Locate every white blood cell.
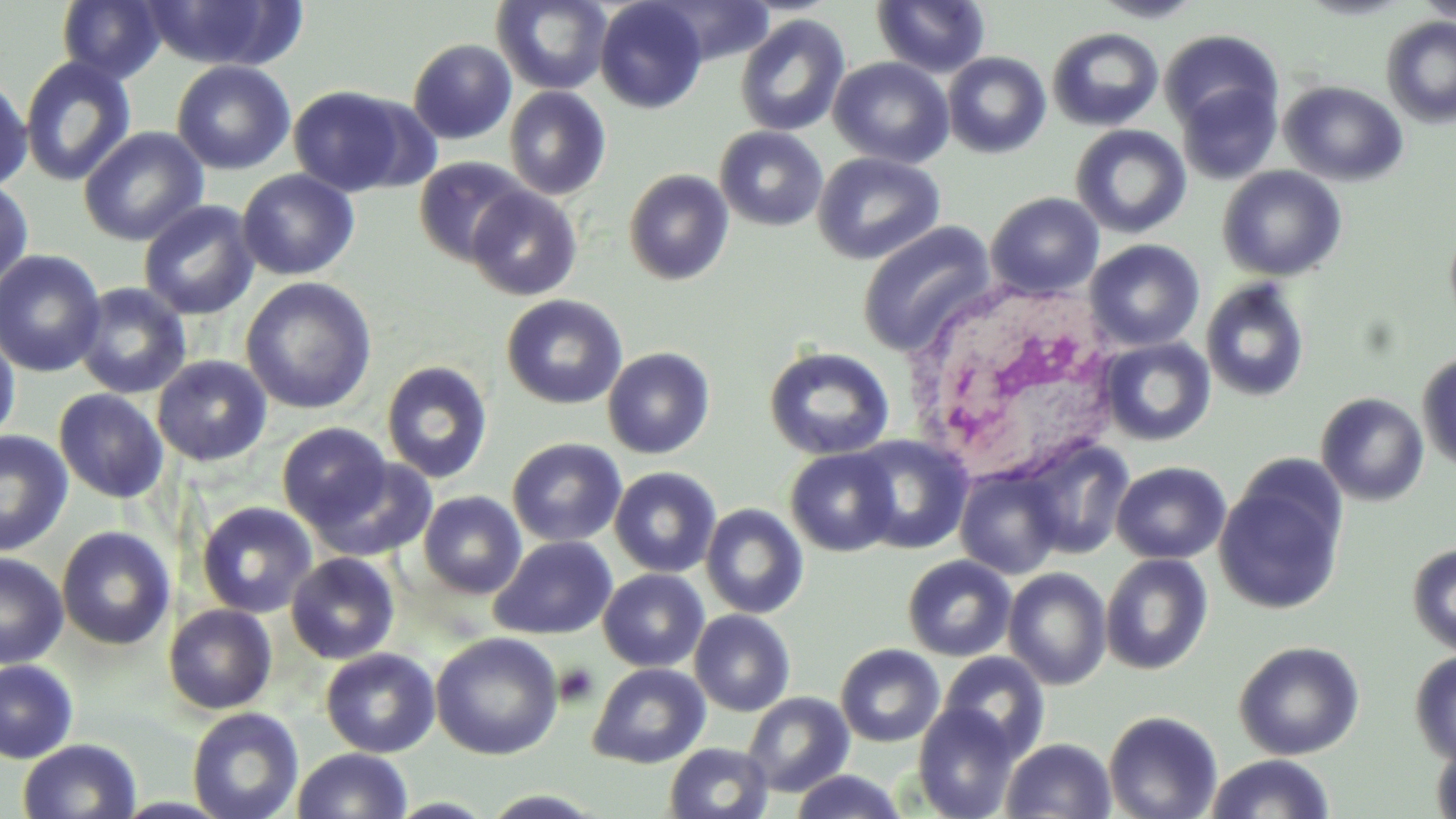
Approximate bounding boxes as [x1, y1, x2, y2] in pixels.
White blood cells: [900, 275, 1134, 494].

Uninfected red blood cell locations: [56, 0, 166, 84], [139, 0, 298, 70], [652, 0, 777, 66], [872, 0, 991, 78], [1091, 0, 1207, 23], [1415, 0, 1456, 22], [491, 1, 613, 94], [595, 1, 708, 113], [734, 14, 851, 137], [1380, 17, 1456, 128], [1047, 27, 1164, 131], [1159, 30, 1284, 134], [408, 39, 517, 144], [942, 51, 1051, 158], [19, 55, 137, 187], [828, 56, 954, 169], [172, 60, 295, 175], [0, 74, 32, 193], [1175, 79, 1282, 184], [1279, 80, 1409, 186], [288, 85, 417, 197], [504, 86, 612, 200], [1070, 124, 1192, 239], [79, 126, 208, 246], [714, 126, 828, 231], [812, 151, 945, 265], [414, 157, 531, 266], [1217, 165, 1347, 281], [237, 169, 359, 280], [623, 169, 734, 286], [0, 178, 34, 294], [466, 186, 583, 301], [985, 192, 1104, 300], [138, 200, 260, 320], [1444, 219, 1456, 337], [857, 221, 998, 356], [1085, 238, 1205, 352], [0, 250, 106, 378], [240, 276, 378, 415], [1200, 277, 1310, 402], [73, 282, 192, 399], [501, 294, 627, 410], [0, 327, 21, 448], [1098, 336, 1216, 446], [763, 346, 895, 461], [602, 347, 715, 459], [1416, 349, 1456, 472], [152, 355, 272, 466], [381, 361, 493, 484], [53, 388, 169, 503], [1315, 392, 1429, 506], [277, 422, 394, 532], [0, 430, 74, 557], [850, 434, 973, 553], [507, 437, 627, 548], [1019, 438, 1134, 559], [786, 447, 900, 556], [310, 455, 437, 561], [1112, 461, 1231, 564], [609, 466, 722, 578], [955, 469, 1064, 579], [1214, 474, 1347, 614], [418, 491, 527, 599], [196, 501, 318, 618], [700, 503, 809, 619], [57, 526, 175, 651], [489, 535, 617, 640], [1407, 543, 1456, 655], [0, 551, 68, 668], [286, 552, 400, 664], [1101, 554, 1213, 675], [902, 555, 1017, 661], [1003, 567, 1112, 690], [598, 569, 709, 672], [162, 603, 278, 715], [689, 609, 796, 716], [431, 632, 564, 760], [1233, 640, 1365, 760], [835, 643, 945, 747], [320, 648, 441, 757], [1409, 650, 1456, 766], [937, 652, 1050, 762], [0, 659, 79, 764], [588, 662, 711, 768], [742, 692, 854, 797], [913, 703, 1020, 819], [187, 707, 304, 819], [1103, 710, 1223, 819], [1429, 736, 1456, 819], [1001, 737, 1117, 818], [17, 738, 142, 819], [664, 742, 773, 819], [292, 748, 413, 819], [1205, 754, 1335, 818], [788, 770, 908, 819]. Platelet locations: [554, 662, 600, 706]. Slide-level diagnosis: no evidence of blood parasites. Thin blood film. Captured at 1000x magnification. Light microscopy. Single field of view. Image is 1456×819 pixels. May-Grünwald-Giemsa-stained preparation.